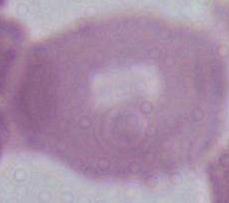
modality = micrograph
identification = erythrocyte
magnification = 1000x